Name the parasite shown.
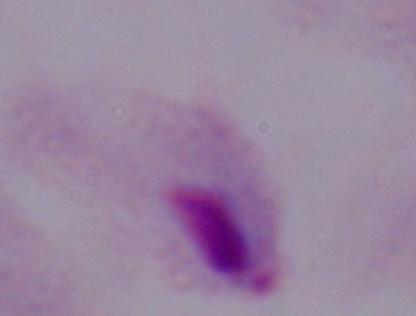

A trichomonad.

{
  "modality": "photomicrograph",
  "magnification": "1000x"
}